Locate and identify every blood parasite.
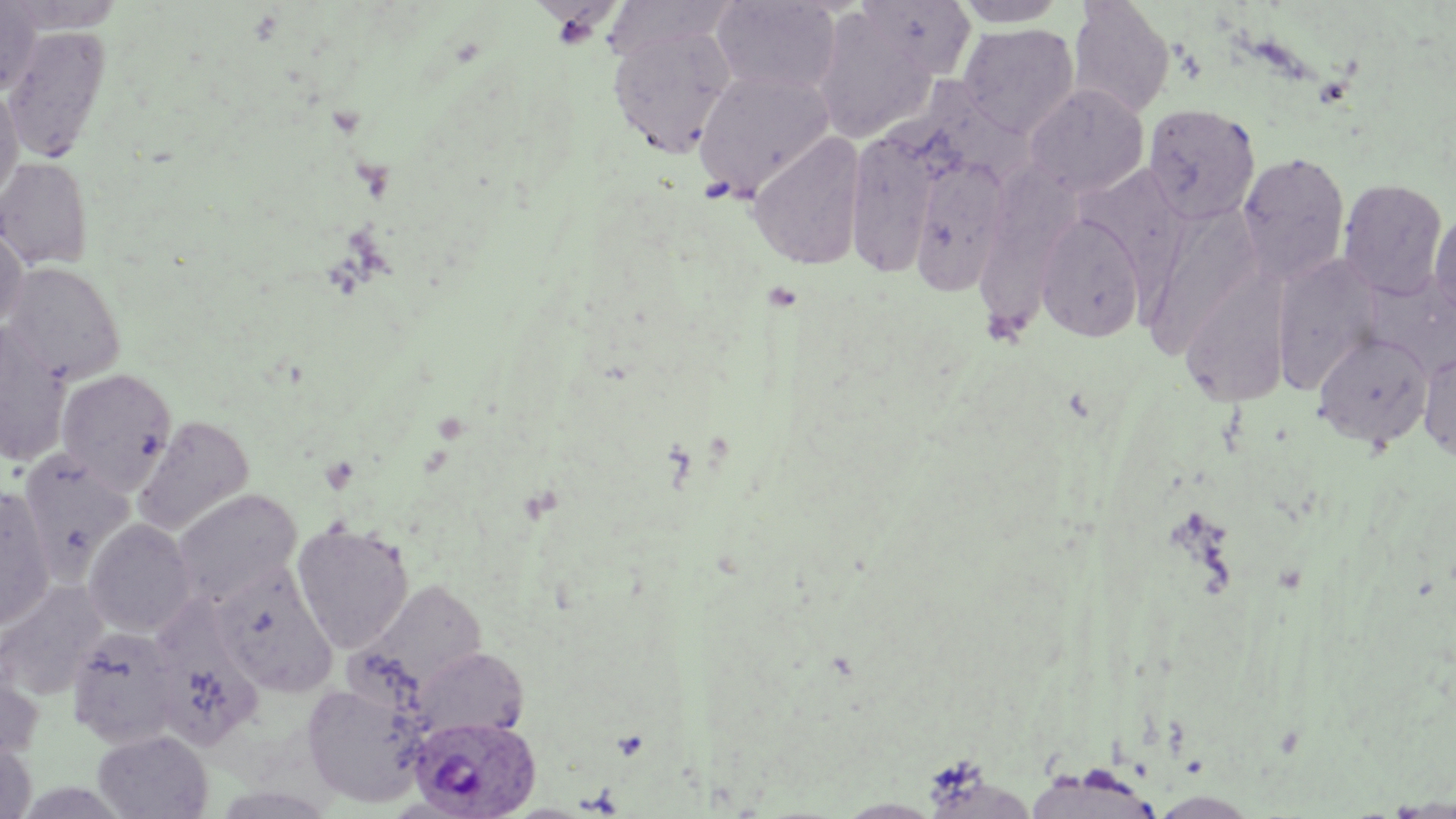

Approximate bounding boxes as (x1, y1, x2, y2) in pixels.
Plasmodium ovale-infected red blood cells: (409, 715, 539, 819).
No Plasmodium falciparum, Plasmodium malariae, Plasmodium vivax, Babesia divergens, or Trypanosoma brucei observed.

Summary:
  - Uninfected red blood cell locations: (709, 0, 843, 97), (854, 0, 978, 79), (0, 1, 41, 95), (951, 1, 1070, 27), (1067, 1, 1175, 120), (5, 3, 124, 32), (810, 9, 936, 144), (607, 20, 738, 159), (957, 24, 1080, 137), (3, 25, 112, 163), (693, 68, 836, 198), (909, 78, 1035, 194), (1023, 83, 1149, 197), (0, 84, 24, 202), (1142, 103, 1261, 225), (844, 122, 946, 279), (747, 131, 868, 271), (906, 151, 1011, 298), (1236, 152, 1350, 284), (0, 156, 94, 269), (981, 156, 1090, 342), (1087, 157, 1195, 322), (1338, 178, 1449, 300), (1146, 208, 1263, 353), (1429, 208, 1456, 324), (1034, 212, 1147, 342), (0, 222, 28, 329), (1271, 254, 1381, 392), (2, 261, 126, 383), (1180, 265, 1292, 407), (1363, 271, 1456, 379), (0, 322, 72, 466), (1313, 331, 1434, 448), (1418, 346, 1456, 463), (56, 367, 177, 493), (133, 416, 254, 537), (18, 450, 135, 577), (0, 485, 56, 631), (171, 488, 302, 607), (82, 519, 198, 637), (292, 522, 414, 653), (213, 565, 338, 696), (0, 580, 108, 700), (369, 580, 488, 693), (151, 605, 260, 751), (66, 625, 184, 748), (410, 646, 529, 743), (0, 664, 44, 765), (301, 678, 430, 808), (92, 729, 213, 818), (0, 738, 37, 818)
  - Slide-level diagnosis: Plasmodium ovale
  - Image size: 1456×819 pixels
  - Field of view: single
  - Modality: optical microscopy
  - Magnification: 1000x
  - Preparation: thin blood smear
  - Stain: May-Grünwald-Giemsa